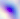
magnification: 400x
modality: micrograph
identification: Toxoplasma gondii